Assess the morphology of the red blood cells.
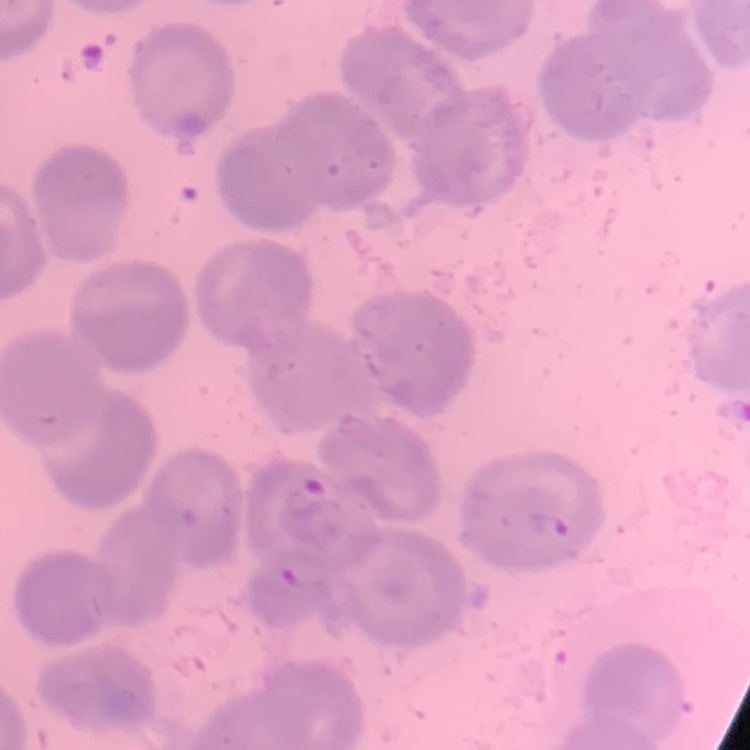
No rouleaux formation.

Thin blood smear. Square crop of a larger photomicrograph. Field's or Giemsa stain.